Give the position of every Plasmodium parasite visible.
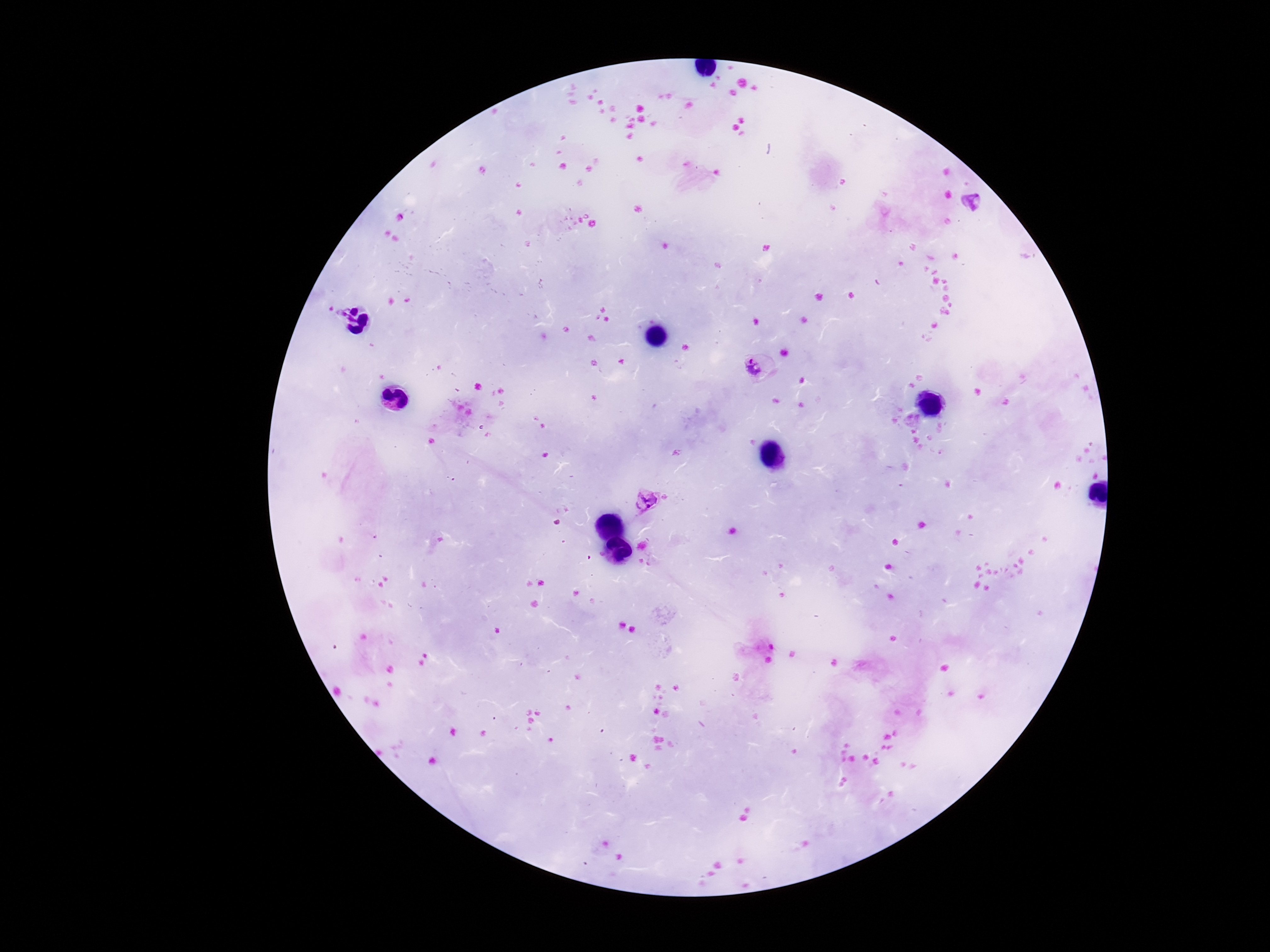
Approximate centers as {x, y} in pixels.
Plasmodium parasites: {970, 202}, {755, 369}, {645, 503}.

Summary:
  - Preparation: thick peripheral-blood smear
  - Capture: smartphone camera through the microscope eyepiece
  - Stain: Giemsa
  - Field of view: one from this slide
  - Patient malaria status: positive
  - Image size: 1270×952 pixels
  - Magnification: 100x